Report the malaria status of this cell.
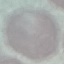

Uninfected.

Photographed with a smartphone camera at the microscope eyepiece. Thin blood smear. Giemsa stain. Cell patch, automatically extracted from a larger field of view and resized to 64 × 64 pixels.